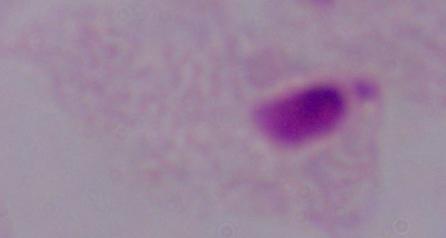

1000x magnification. Photomicrograph. A trichomonad is shown.